Report the malaria status of this cell.
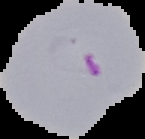
It is parasitized.

Cell region segmented out of the field of view; the surrounding area is masked to black. Image is 145×139 pixels. From a thin blood film.